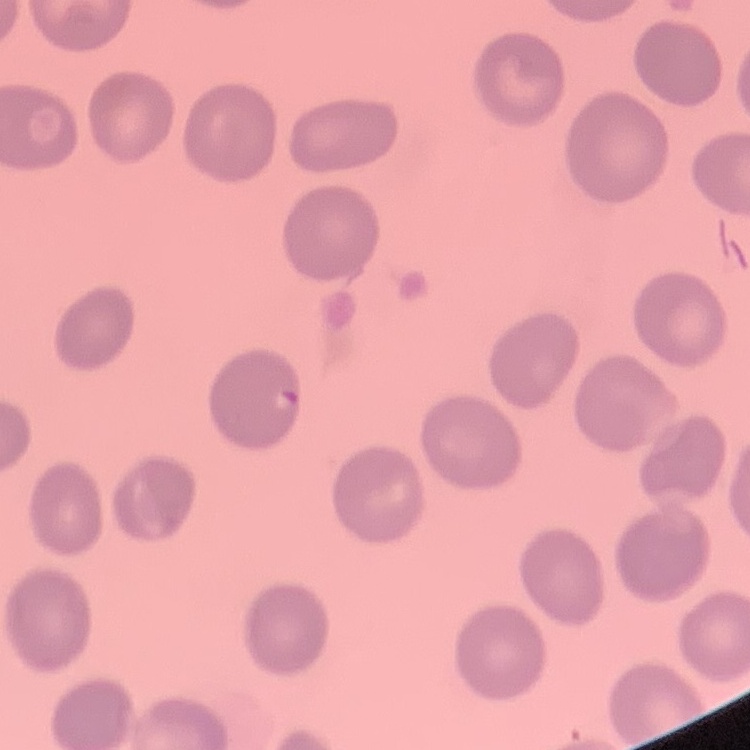

red blood cell morphology = no rouleaux formation
image type = one tile cut from a larger photomicrograph
stain = Field's or Giemsa
preparation = thin peripheral smear